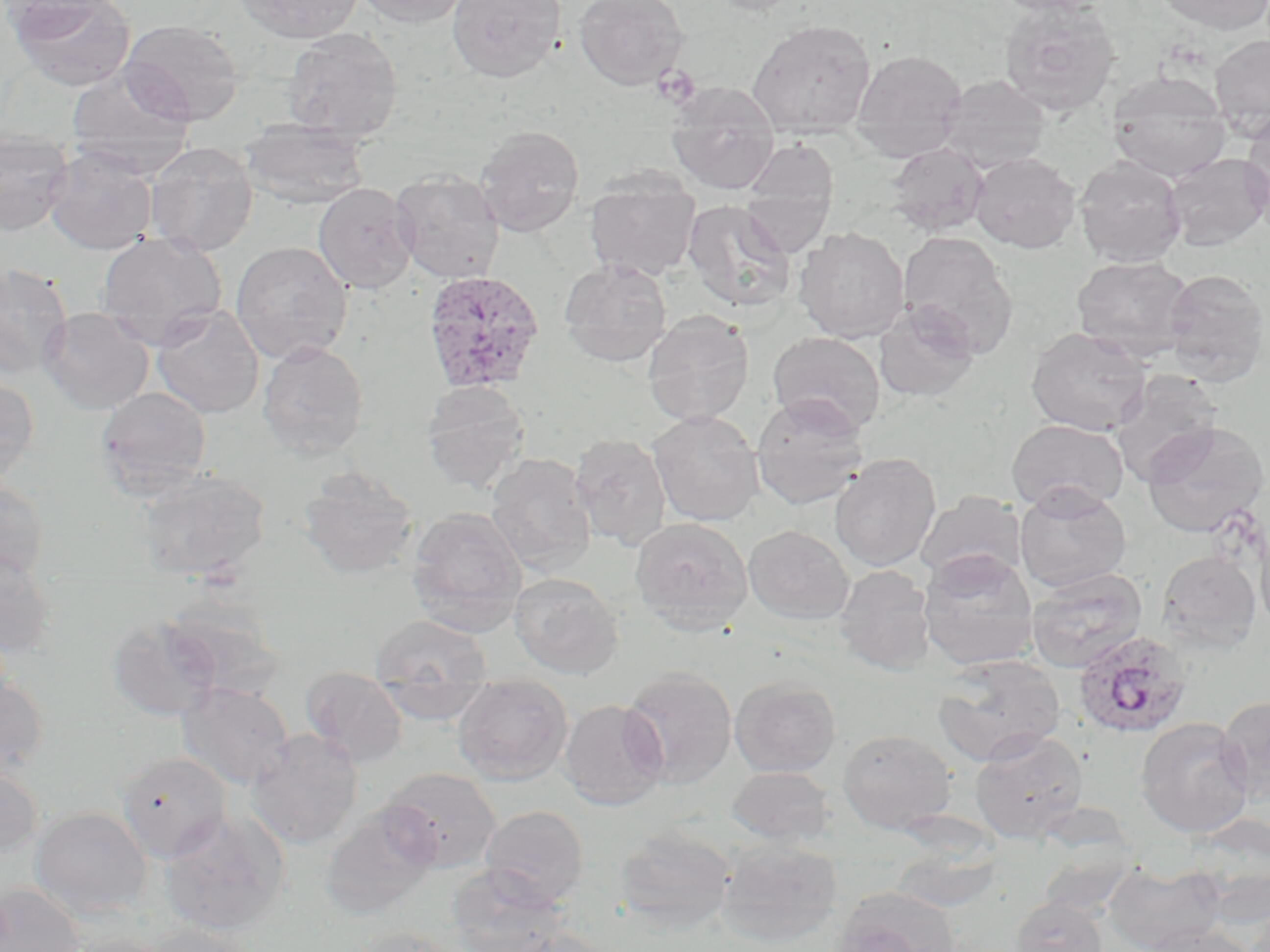

Summary:
  - Coordinate format: approximate bounding boxes as (x1,y1)-(x2,y2) corner pairs in pixels
  - Platelet locations: (651,65)-(701,108)
  - Uninfected red blood cell locations: (0,0)-(116,41), (10,0)-(136,91), (234,0)-(365,43), (353,0)-(474,28), (447,0)-(566,83), (575,0)-(689,90), (707,0)-(807,15), (989,0)-(1111,16), (1156,0)-(1270,34), (999,2)-(1120,116), (120,19)-(245,126), (747,19)-(877,139), (282,27)-(403,143), (1209,35)-(1270,137), (850,49)-(968,161), (65,66)-(196,176), (1107,71)-(1232,183), (937,74)-(1051,173), (666,83)-(780,194), (1241,113)-(1270,230), (240,120)-(371,209), (475,125)-(584,236), (0,130)-(74,236), (743,139)-(839,216), (887,141)-(990,237), (146,142)-(258,257), (44,146)-(158,255), (969,151)-(1080,253), (1163,152)-(1270,252), (1074,156)-(1187,268), (390,171)-(506,283), (584,173)-(701,281), (313,183)-(417,294), (740,188)-(835,257), (681,199)-(797,312), (794,226)-(910,343), (897,230)-(1018,357), (96,231)-(227,346), (230,241)-(352,364), (1071,255)-(1196,361), (559,259)-(672,367), (0,261)-(73,381), (1161,268)-(1269,387), (873,301)-(981,404), (152,305)-(264,419), (38,307)-(154,414), (642,311)-(754,426), (1026,326)-(1153,435), (767,331)-(886,436), (257,341)-(369,460), (1110,370)-(1224,484), (0,377)-(39,488), (421,380)-(530,494), (94,386)-(212,499), (751,395)-(870,511), (647,410)-(765,527), (1006,418)-(1129,514), (1142,421)-(1268,537), (570,433)-(672,552), (486,452)-(597,577), (829,452)-(941,572), (298,466)-(419,580), (133,469)-(271,583), (0,476)-(50,582), (1014,485)-(1132,593), (915,491)-(1027,585), (408,506)-(527,633), (1255,515)-(1270,638), (630,517)-(753,634), (744,525)-(855,625), (919,549)-(1039,671), (0,550)-(59,659), (1156,550)-(1262,653), (834,565)-(936,675), (1026,568)-(1148,672), (509,572)-(624,679), (161,595)-(287,698), (371,614)-(491,684), (107,617)-(222,721), (932,654)-(1065,766), (619,667)-(738,787), (300,669)-(408,767), (0,674)-(50,781), (730,677)-(841,777), (453,681)-(573,784), (177,682)-(294,791), (374,684)-(494,723), (1216,695)-(1270,805), (559,699)-(667,810), (1134,716)-(1254,837), (838,729)-(957,833), (970,729)-(1088,841), (246,730)-(363,849), (115,750)-(233,863), (0,762)-(43,860), (726,766)-(835,845), (381,767)-(503,873), (319,805)-(440,920), (480,805)-(589,908), (31,806)-(153,919), (159,812)-(289,938), (615,828)-(737,933), (716,838)-(845,947), (889,844)-(1004,913), (1104,861)-(1226,952), (446,865)-(569,952), (0,883)-(85,952), (831,887)-(961,952), (1011,897)-(1108,952), (141,923)-(259,952), (1142,924)-(1258,952), (349,927)-(463,952), (502,928)-(615,952), (60,933)-(179,952)
  - Plasmodium ovale-infected red blood cell locations: (422,270)-(545,394), (1073,630)-(1193,738)
  - Slide-level diagnosis: Plasmodium ovale
  - Image size: 1270×952 pixels
  - Magnification: 1000x
  - Preparation: thin blood smear
  - Modality: light microscopy
  - Stain: May-Grünwald-Giemsa
  - Field of view: single